Classify this cell by malaria status.
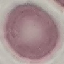

It is uninfected.

Giemsa-stained preparation. Thin smear of blood. Photographed with a smartphone camera at the microscope eyepiece. Automatically extracted cell patch, resized to 64 × 64 pixels.